Assess this cell for malaria.
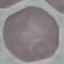

Uninfected.

Summary:
  - Preparation: thin blood smear
  - Capture: smartphone through the microscope eyepiece
  - Stain: Giemsa
  - Image type: cell patch, automatically extracted from a larger field of view and resized to 64 × 64 pixels